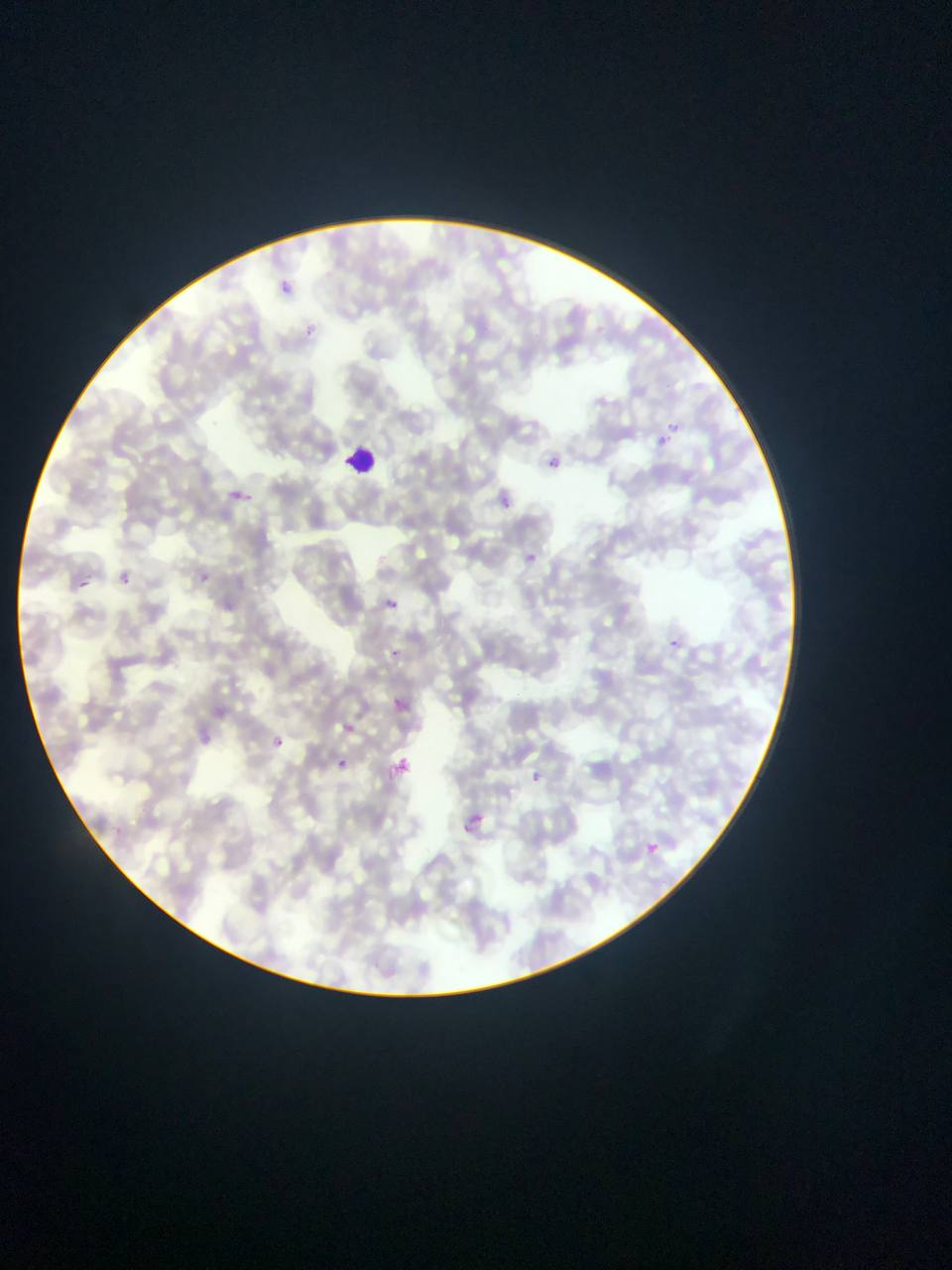 Approximate bounding boxes as (left, top, right, bottom) in pixels. Malaria parasite locations: (279, 278, 297, 296), (302, 326, 318, 338), (667, 421, 678, 433), (658, 433, 670, 447), (547, 455, 559, 468), (228, 485, 251, 506), (499, 495, 511, 510), (525, 550, 543, 563), (120, 573, 130, 584), (199, 573, 213, 583), (78, 580, 87, 587), (380, 596, 405, 604), (672, 632, 682, 650), (390, 650, 399, 658), (395, 698, 417, 720), (345, 724, 354, 732), (274, 737, 284, 747), (338, 758, 348, 767), (526, 765, 545, 785), (459, 823, 477, 837), (646, 841, 664, 857). Leukocyte locations: (342, 442, 381, 478). Photographed through a microscope with a mobile-phone camera. Single field of view. Collected in Ghana. Image is 952×1270 pixels. Thin blood smear.